Report the malaria status of this cell.
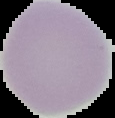

It is uninfected.

Image is 115×118 pixels. Cell region segmented out of the field of view; the surrounding area is masked to black. From a thin blood smear.